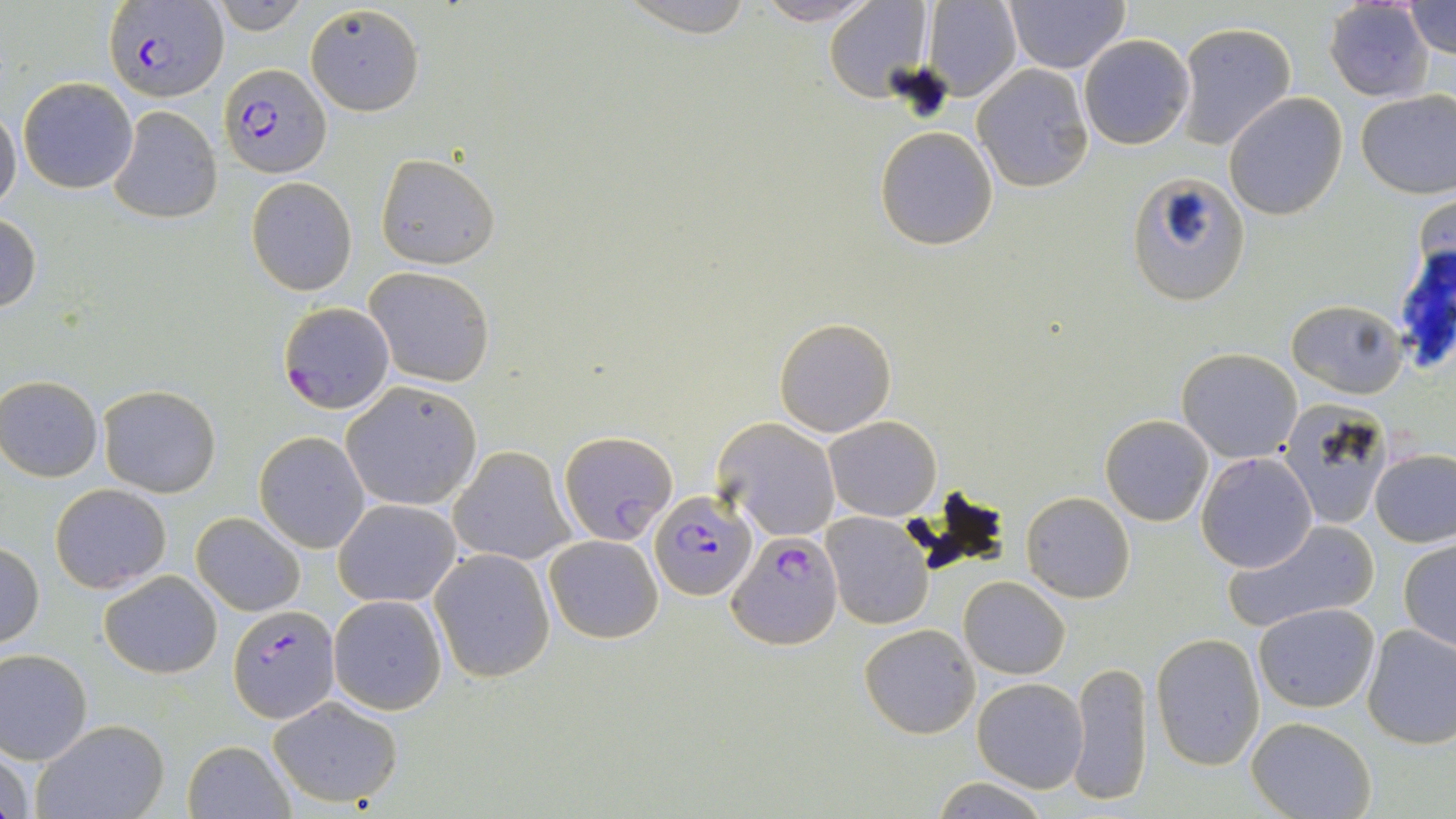
Approximate bounding boxes as (x1, y1, x2, y2) in pixels. Uninfected red blood cell locations: (620, 0, 755, 35), (750, 0, 879, 25), (1005, 0, 1130, 73), (210, 1, 307, 34), (825, 1, 933, 100), (922, 1, 1021, 100), (1325, 1, 1433, 101), (1404, 2, 1456, 60), (304, 3, 425, 116), (1173, 21, 1297, 152), (1079, 35, 1193, 149), (972, 64, 1092, 192), (18, 77, 138, 194), (1356, 88, 1455, 197), (1223, 93, 1347, 221), (0, 104, 22, 215), (108, 105, 222, 225), (875, 126, 999, 250), (375, 154, 499, 270), (1127, 173, 1249, 304), (247, 178, 357, 295), (0, 214, 42, 315), (364, 266, 495, 387), (1285, 297, 1408, 399), (773, 316, 897, 438), (1177, 347, 1302, 462), (0, 375, 104, 482), (341, 381, 483, 511), (96, 385, 221, 497), (1276, 400, 1397, 525), (1100, 414, 1212, 526), (825, 415, 941, 521), (714, 418, 841, 541), (254, 431, 371, 552), (450, 446, 573, 566), (1370, 449, 1456, 548), (1195, 452, 1319, 573), (50, 483, 171, 593), (1022, 492, 1135, 603), (334, 497, 460, 607), (191, 511, 305, 616), (822, 512, 933, 630), (1222, 518, 1379, 634), (544, 535, 664, 643), (1398, 539, 1456, 652), (0, 543, 45, 649), (431, 550, 555, 683), (99, 570, 223, 679), (959, 575, 1070, 679), (329, 595, 447, 714), (1255, 602, 1380, 713), (1265, 614, 1454, 735), (859, 623, 979, 738), (1362, 623, 1456, 748), (1152, 632, 1267, 768), (0, 648, 93, 763), (1068, 659, 1153, 807), (972, 677, 1088, 792), (268, 696, 404, 809), (1246, 716, 1376, 819), (34, 719, 166, 819), (182, 739, 294, 818), (0, 740, 35, 819), (930, 778, 1051, 817). Plasmodium falciparum-infected red blood cell locations: (103, 1, 226, 102), (219, 62, 330, 180), (277, 302, 395, 413), (559, 431, 678, 544), (651, 488, 756, 601), (731, 530, 843, 648), (229, 604, 339, 721). Slide-level diagnosis: Plasmodium falciparum. Image is 1456×819 pixels. Optical microscopy. 1000x magnification. May-Grünwald-Giemsa stain. Thin blood smear. One field of a larger specimen.